Name the parasite shown.
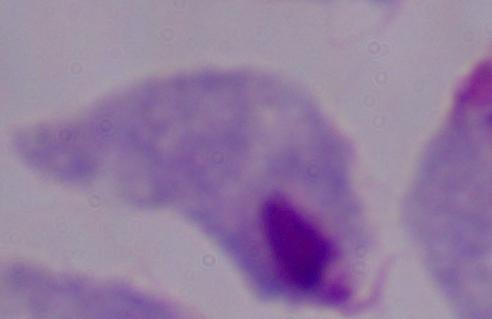
A trichomonad.

Micrograph. Captured at 1000x magnification.